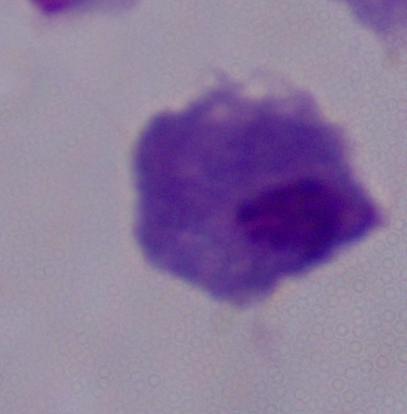
Summary:
  - Modality: micrograph
  - Magnification: 1000x
  - Identification: trichomonad